Classify this cell by malaria status.
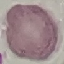
It is uninfected.

Summary:
  - Stain: Giemsa
  - Preparation: thin blood smear
  - Image type: automatically extracted cell patch, resized to 64 × 64 pixels
  - Capture: smartphone camera at the microscope eyepiece